Outline each blood parasite and name the species.
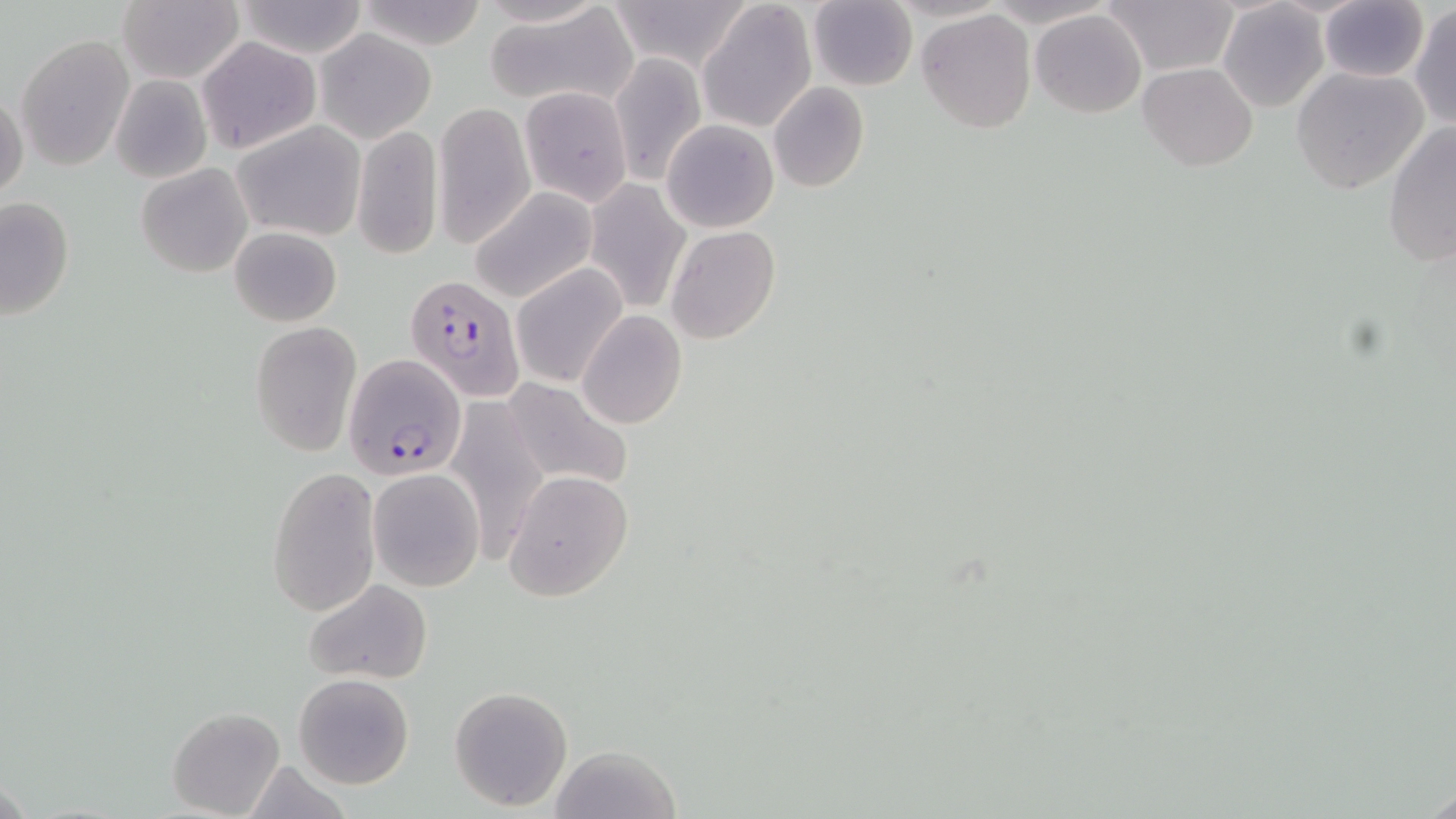

Approximate bounding boxes as (x1, y1, x2, y2) in pixels.
Plasmodium falciparum-infected red blood cells: (407, 275, 523, 401), (345, 355, 469, 479).
No Plasmodium ovale, Plasmodium malariae, Plasmodium vivax, Babesia divergens, or Trypanosoma brucei observed.

slide-level diagnosis = Plasmodium falciparum
modality = light microscopy
image size = 1456×819 pixels
field of view = single
preparation = thin blood smear
stain = May-Grünwald-Giemsa
uninfected red blood cell locations = approximate bounding boxes as (x1, y1, x2, y2) in pixels: (232, 0, 370, 57), (352, 0, 493, 48), (611, 0, 753, 71), (1102, 0, 1239, 76), (1319, 0, 1428, 82), (115, 1, 243, 84), (698, 1, 816, 132), (808, 1, 919, 91), (1217, 3, 1330, 113), (483, 5, 639, 110), (1410, 5, 1456, 129), (917, 9, 1037, 134), (1030, 9, 1146, 117), (315, 30, 435, 142), (16, 34, 135, 171), (196, 36, 321, 155), (610, 53, 706, 184), (1137, 63, 1258, 170), (1290, 67, 1431, 193), (110, 73, 213, 183), (768, 83, 870, 194), (0, 87, 28, 204), (519, 87, 634, 206), (433, 100, 535, 248), (233, 120, 367, 242), (661, 120, 778, 233), (1383, 122, 1455, 266), (352, 125, 442, 260), (135, 163, 252, 277), (583, 179, 691, 311), (469, 188, 596, 303), (0, 197, 75, 320), (229, 226, 342, 327), (665, 226, 780, 345), (511, 264, 627, 387), (577, 311, 686, 429), (251, 321, 360, 454), (505, 377, 635, 493), (449, 398, 547, 550), (267, 466, 379, 619), (367, 468, 485, 591), (501, 469, 634, 603), (304, 578, 433, 685), (293, 674, 414, 789), (449, 685, 573, 811), (167, 705, 285, 817), (549, 744, 680, 819)
magnification = 1000x